Identify the parasite.
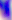
Toxoplasma gondii.

modality = photomicrograph
magnification = 400x